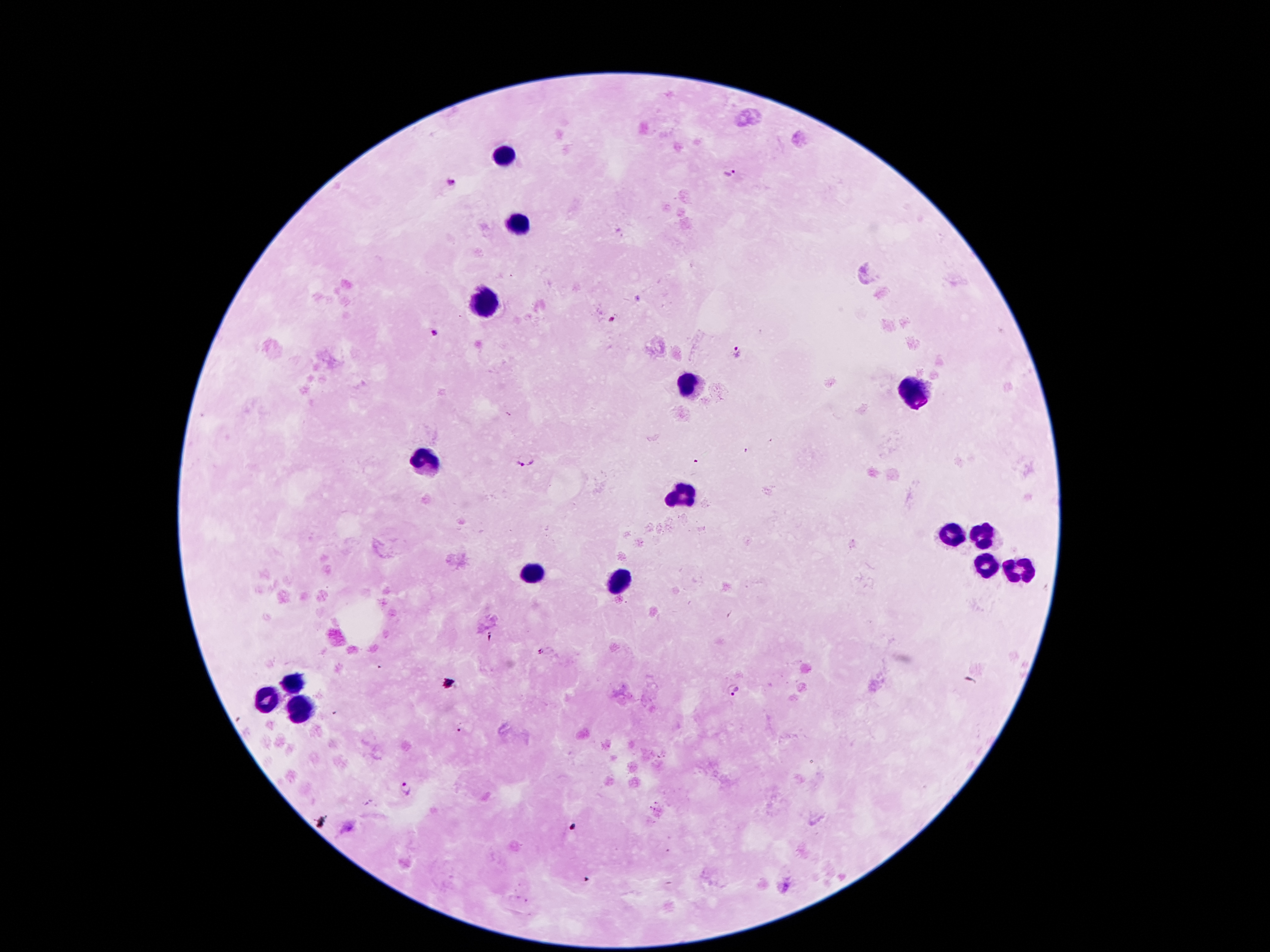

Approximate centers as [x, y] in pixels.
Summary:
  - Leukocyte locations: [503, 156], [517, 223], [486, 303], [689, 383], [916, 389], [427, 460], [685, 496], [979, 536], [948, 538], [986, 565], [532, 574], [1017, 576], [622, 582], [295, 683], [265, 697], [299, 710]
  - Malaria parasite locations: [731, 174], [450, 182], [613, 322], [433, 334], [737, 353], [523, 462], [736, 692], [460, 728], [405, 789]
  - Magnification: 100x
  - Patient malaria status: infected with Plasmodium falciparum
  - Field of view: one from this slide
  - Capture: smartphone through the microscope eyepiece
  - Stain: Giemsa
  - Image size: 1270×952 pixels
  - Preparation: thick peripheral-blood smear